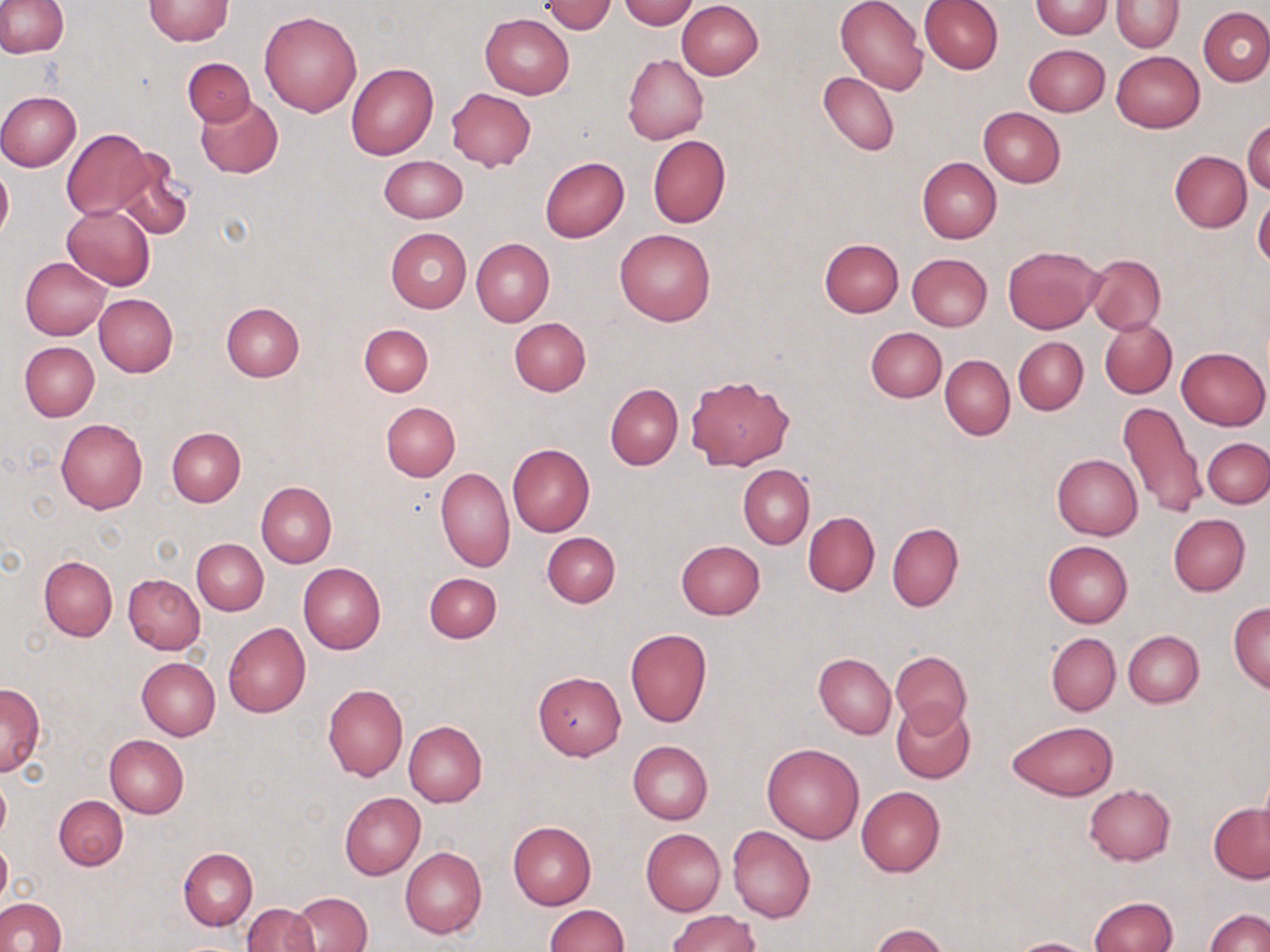
slide-level diagnosis = negative for blood parasites
stain = May-Grünwald-Giemsa
field of view = single
uninfected red blood cell locations = approximate bounding boxes as [x1, y1, x2, y2] in pixels: [0, 0, 68, 58], [618, 0, 698, 29], [836, 0, 928, 97], [919, 0, 1003, 74], [1112, 0, 1183, 50], [143, 1, 233, 45], [676, 1, 763, 80], [1029, 1, 1112, 38], [542, 2, 617, 34], [1199, 6, 1270, 87], [259, 10, 363, 117], [480, 14, 574, 99], [1023, 44, 1109, 117], [1111, 51, 1204, 132], [622, 54, 707, 144], [182, 58, 255, 126], [346, 63, 438, 160], [819, 71, 899, 156], [447, 87, 536, 171], [0, 90, 81, 172], [195, 96, 283, 179], [978, 107, 1065, 187], [1244, 118, 1270, 196], [62, 128, 154, 220], [647, 134, 731, 228], [114, 151, 193, 242], [1170, 151, 1251, 233], [379, 155, 467, 222], [917, 156, 1002, 243], [539, 157, 629, 243], [0, 163, 13, 245], [1253, 194, 1270, 272], [61, 205, 155, 291], [385, 227, 472, 312], [615, 229, 715, 325], [471, 238, 554, 326], [818, 238, 904, 317], [1003, 245, 1104, 334], [1011, 248, 1092, 415], [907, 253, 992, 331], [1085, 254, 1166, 335], [21, 257, 111, 340], [94, 293, 178, 376], [221, 302, 305, 382], [509, 317, 592, 395], [1100, 317, 1177, 398], [359, 323, 433, 396], [866, 327, 947, 402], [1014, 337, 1087, 413], [19, 341, 99, 422], [1176, 346, 1269, 430], [940, 354, 1015, 441], [685, 373, 795, 469], [606, 383, 683, 470], [381, 401, 460, 480], [1117, 401, 1206, 521], [55, 419, 147, 513], [167, 428, 245, 506], [1202, 437, 1269, 508], [508, 444, 595, 537], [1052, 454, 1143, 540], [739, 465, 814, 548], [436, 468, 515, 571], [257, 482, 337, 567], [803, 511, 880, 596], [1168, 514, 1251, 595], [887, 522, 964, 611], [542, 531, 620, 607], [192, 538, 268, 615], [675, 540, 765, 619], [1043, 541, 1133, 628], [39, 556, 117, 641], [298, 562, 386, 653], [424, 571, 502, 643], [123, 573, 206, 653], [1229, 603, 1270, 692], [223, 622, 312, 718], [625, 628, 712, 728], [1122, 630, 1203, 708], [1046, 632, 1121, 715], [890, 651, 970, 731], [813, 653, 895, 738], [137, 657, 220, 739], [533, 671, 626, 759], [0, 682, 45, 776], [322, 683, 408, 780], [891, 700, 977, 784], [404, 720, 487, 808], [1008, 720, 1119, 800], [104, 733, 189, 817], [628, 741, 712, 824], [762, 743, 865, 843], [1256, 766, 1270, 854], [0, 774, 11, 847], [1084, 784, 1176, 865], [856, 786, 945, 877], [340, 792, 426, 880], [54, 795, 128, 870], [1209, 804, 1270, 883], [508, 822, 596, 909], [727, 826, 815, 924], [641, 829, 726, 915], [0, 838, 11, 910], [401, 846, 486, 938], [178, 847, 257, 930], [291, 891, 372, 952], [1089, 897, 1179, 952], [0, 898, 68, 952], [243, 902, 318, 952], [543, 904, 627, 952], [668, 909, 760, 951], [1204, 909, 1270, 952], [870, 924, 949, 952], [1006, 938, 1099, 952]
image size = 1270×952 pixels
magnification = 1000x
modality = optical microscopy
preparation = thin blood film